Locate every blood parasite and identify its species.
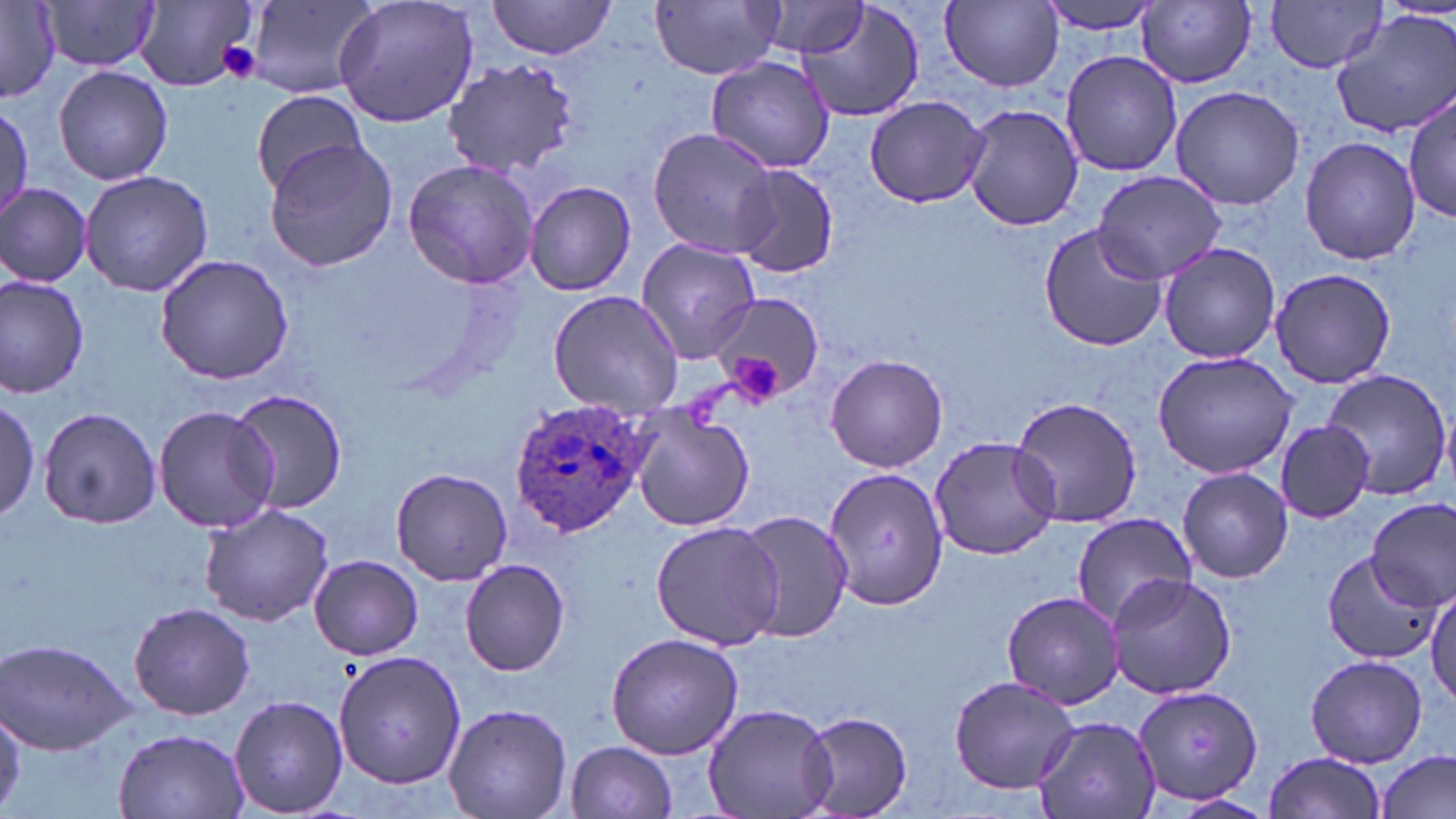

Approximate bounding boxes as (x1, y1, x2, y2) in pixels.
Plasmodium ovale-infected red blood cells: (508, 397, 651, 538).
No Plasmodium falciparum, Plasmodium malariae, Plasmodium vivax, Babesia divergens, or Trypanosoma brucei observed.

slide-level diagnosis = Plasmodium ovale
image size = 1456×819 pixels
uninfected red blood cell locations = approximate bounding boxes as (x1, y1, x2, y2) in pixels: (333, 0, 482, 127), (652, 0, 785, 80), (794, 0, 926, 123), (942, 0, 1063, 89), (1039, 0, 1167, 37), (1267, 0, 1388, 74), (41, 1, 160, 72), (137, 1, 261, 90), (246, 1, 380, 97), (757, 1, 871, 57), (1137, 1, 1258, 87), (485, 2, 617, 58), (0, 3, 60, 100), (1333, 10, 1456, 138), (1059, 50, 1181, 176), (705, 56, 836, 173), (440, 58, 584, 175), (54, 66, 173, 186), (1168, 83, 1307, 209), (250, 88, 369, 197), (1405, 92, 1454, 225), (865, 96, 988, 207), (0, 102, 31, 222), (961, 102, 1084, 232), (647, 127, 777, 258), (1299, 135, 1422, 265), (263, 138, 398, 271), (400, 158, 539, 288), (730, 166, 840, 277), (80, 168, 217, 297), (1090, 169, 1226, 283), (524, 180, 638, 297), (0, 183, 92, 288), (1037, 223, 1169, 352), (636, 239, 761, 361), (1158, 242, 1281, 363), (153, 254, 297, 387), (1268, 267, 1400, 389), (0, 275, 90, 397), (547, 288, 684, 418), (701, 293, 826, 403), (1152, 351, 1298, 480), (824, 353, 950, 473), (1319, 369, 1453, 502), (227, 387, 350, 515), (1005, 394, 1142, 535), (0, 397, 45, 523), (153, 405, 279, 534), (628, 405, 755, 532), (39, 407, 162, 530), (1274, 419, 1377, 523), (927, 433, 1062, 561), (819, 465, 948, 610), (1177, 467, 1294, 583), (390, 468, 512, 585), (1367, 500, 1455, 611), (198, 501, 335, 626), (731, 508, 853, 643), (1069, 512, 1196, 628), (650, 519, 784, 649), (1324, 550, 1438, 663), (309, 554, 423, 660), (460, 559, 570, 676), (1106, 571, 1240, 699), (1428, 587, 1456, 707), (1000, 590, 1127, 710), (127, 602, 255, 718), (604, 632, 745, 760), (2, 638, 132, 754), (332, 648, 466, 791), (1304, 653, 1429, 767), (947, 674, 1079, 792), (1131, 684, 1263, 808), (229, 695, 349, 817), (441, 701, 574, 819), (1, 703, 25, 813), (701, 703, 837, 819), (796, 712, 914, 819), (1031, 717, 1162, 819), (114, 727, 249, 818), (564, 740, 678, 818), (1377, 749, 1455, 819), (1261, 752, 1389, 818)
preparation = thin blood smear
stain = May-Grünwald-Giemsa
magnification = 1000x
platelet locations = approximate bounding boxes as (x1, y1, x2, y2) in pixels: (215, 39, 264, 83), (727, 350, 783, 402)
modality = light microscopy
field of view = one of a larger specimen